State the blood parasite species.
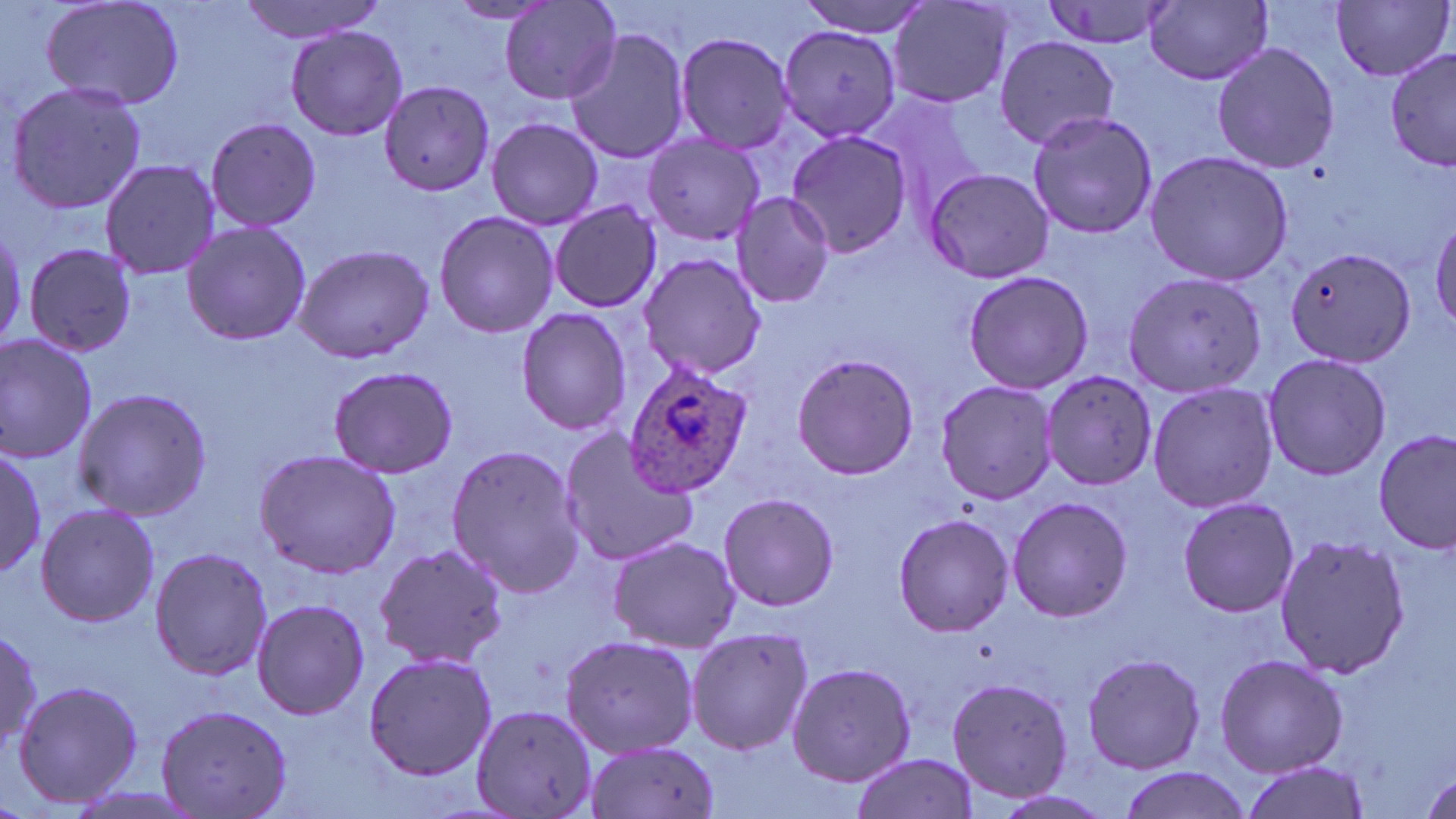

Plasmodium ovale.

Approximate bounding boxes as (x1, y1, x2, y2) in pixels. Plasmodium ovale-infected red blood cell locations: (620, 357, 755, 498). Uninfected red blood cell locations: (38, 0, 186, 112), (239, 0, 388, 42), (794, 0, 933, 37), (1038, 0, 1177, 52), (1331, 0, 1453, 82), (501, 1, 623, 106), (887, 1, 1017, 111), (444, 2, 560, 26), (1145, 2, 1274, 86), (285, 25, 407, 141), (563, 25, 692, 165), (777, 26, 901, 141), (672, 30, 799, 156), (993, 37, 1120, 150), (1210, 40, 1340, 176), (1385, 48, 1456, 173), (4, 80, 150, 216), (377, 80, 495, 199), (862, 91, 995, 222), (1024, 110, 1160, 240), (487, 116, 604, 231), (202, 117, 322, 233), (785, 131, 914, 258), (642, 133, 767, 245), (1143, 150, 1294, 286), (99, 158, 221, 280), (923, 169, 1055, 282), (731, 192, 835, 309), (548, 201, 661, 313), (432, 209, 558, 339), (1429, 215, 1456, 332), (180, 221, 311, 347), (22, 241, 138, 354), (290, 243, 436, 363), (1282, 246, 1418, 368), (638, 251, 771, 382), (1120, 263, 1267, 395), (961, 270, 1094, 395), (514, 308, 631, 434), (0, 331, 100, 463), (1261, 351, 1392, 481), (790, 353, 919, 480), (326, 363, 459, 480), (1040, 371, 1159, 493), (934, 380, 1060, 504), (1146, 381, 1281, 516), (70, 386, 212, 520), (555, 425, 701, 567), (1375, 431, 1454, 556), (444, 442, 586, 598), (0, 447, 46, 578), (252, 449, 403, 578), (718, 492, 839, 610), (1176, 496, 1300, 618), (1007, 497, 1133, 622), (35, 502, 159, 628), (891, 513, 1015, 638), (1273, 531, 1410, 680), (606, 535, 740, 652), (372, 542, 510, 670), (148, 546, 273, 682), (250, 597, 371, 719), (0, 624, 44, 754), (685, 626, 814, 756), (559, 633, 699, 757), (362, 649, 496, 781), (1080, 650, 1207, 774), (1214, 653, 1348, 777), (786, 661, 916, 788), (946, 677, 1074, 802), (10, 679, 145, 811), (154, 703, 293, 819), (471, 703, 597, 819), (583, 738, 722, 819), (850, 753, 981, 819), (1237, 761, 1368, 819), (1115, 767, 1251, 819). Thin blood film. May-Grünwald-Giemsa stain. 1000x magnification. Image is 1456×819 pixels. Light microscopy. One field of a larger specimen.